Classify this cell by malaria status.
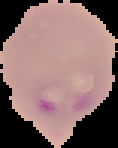
It is parasitized.

Image is 118×148 pixels. The area outside the segmented cell region is set to black. From a thin blood film.